Assess this cell for malaria.
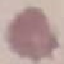
Uninfected.

Thin smear of blood. Giemsa stain. Automatically extracted cell patch, resized to 64 × 64 pixels. Acquired by smartphone through the microscope eyepiece.